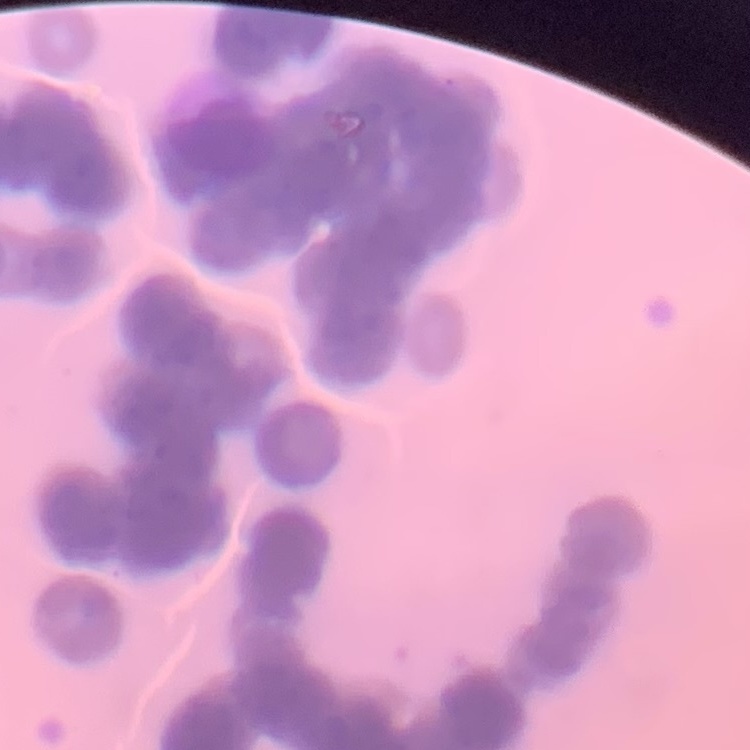
Summary:
  - Red blood cell morphology: rouleaux formation
  - Image type: square crop of a larger photomicrograph
  - Preparation: thin blood smear
  - Stain: Field's or Giemsa